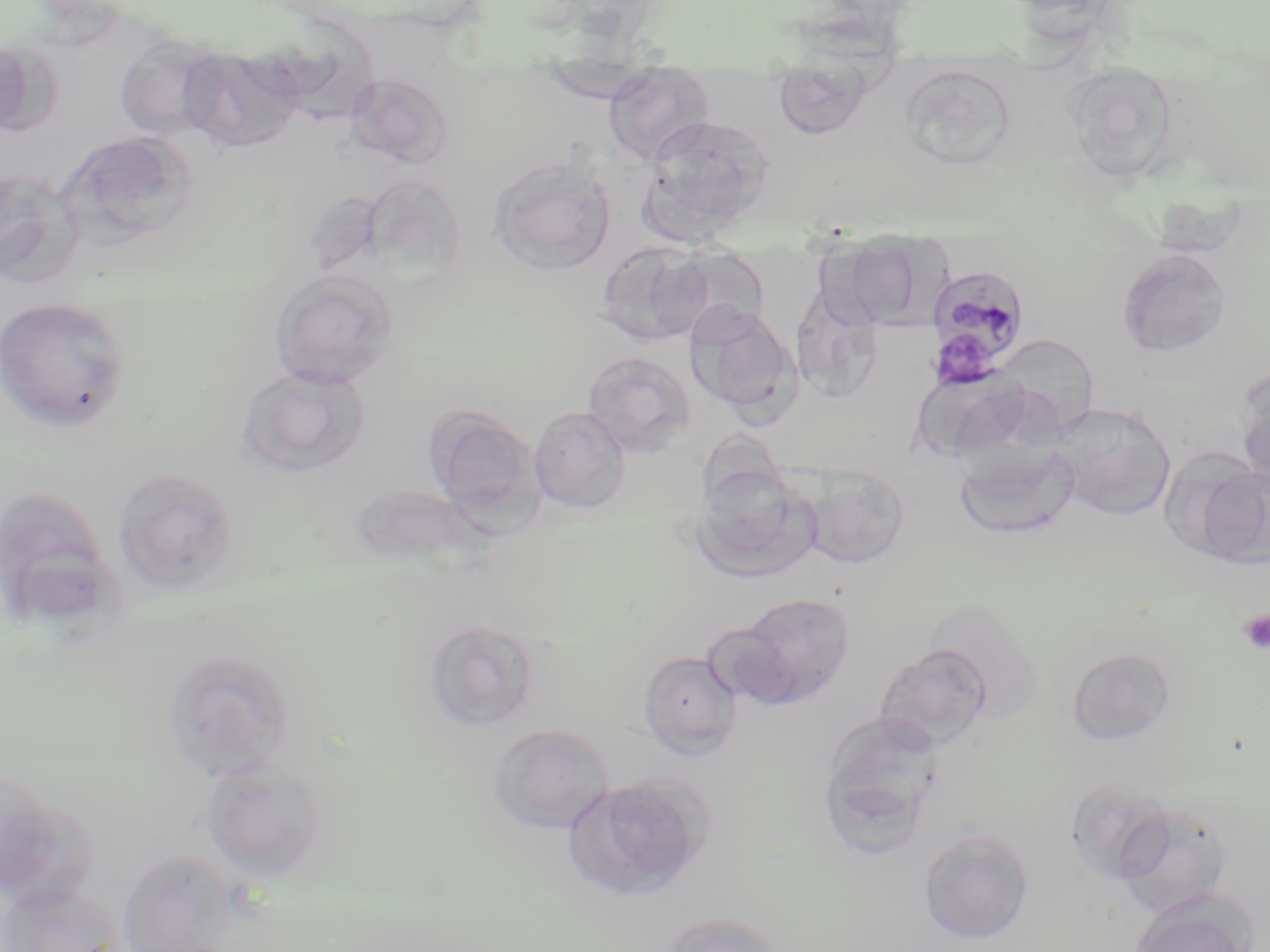

slide-level diagnosis = Plasmodium malariae
field of view = one of a larger specimen
preparation = thin blood film
uninfected red blood cell locations = approximate bounding boxes as [x1, y1, x2, y2] in pixels: [115, 33, 228, 141], [0, 39, 41, 137], [179, 45, 305, 153], [536, 64, 663, 102], [603, 66, 716, 165], [902, 66, 1014, 167], [1059, 67, 1182, 182], [772, 70, 877, 140], [343, 72, 453, 169], [641, 113, 774, 235], [61, 132, 198, 250], [488, 157, 616, 275], [0, 166, 85, 290], [361, 174, 468, 281], [827, 233, 937, 328], [595, 240, 715, 347], [590, 242, 703, 459], [1117, 247, 1233, 360], [269, 270, 399, 389], [790, 286, 885, 404], [0, 297, 130, 432], [686, 305, 802, 419], [1001, 339, 1099, 447], [583, 351, 696, 458], [237, 363, 372, 480], [1235, 366, 1270, 488], [921, 372, 1031, 471], [1053, 402, 1177, 521], [424, 405, 544, 530], [529, 406, 631, 515], [954, 441, 1080, 541], [1178, 455, 1270, 572], [800, 465, 911, 569], [112, 466, 240, 597], [689, 470, 821, 586], [346, 483, 487, 571], [0, 484, 120, 634], [736, 592, 857, 705], [921, 598, 1045, 723], [421, 618, 543, 733], [874, 644, 992, 753], [1066, 646, 1176, 746], [161, 649, 296, 781], [637, 649, 742, 759], [816, 713, 945, 859], [488, 724, 614, 834], [201, 758, 327, 883], [563, 773, 714, 904], [1064, 778, 1178, 885], [0, 786, 97, 910], [1113, 800, 1233, 917], [917, 828, 1036, 944], [117, 849, 240, 952], [0, 884, 124, 952], [1128, 891, 1258, 952], [658, 913, 790, 952]
image size = 1270×952 pixels
magnification = 1000x
Plasmodium malariae-infected red blood cell locations = approximate bounding boxes as [x1, y1, x2, y2] in pixels: [926, 263, 1030, 379]
stain = May-Grünwald-Giemsa
modality = light microscopy
platelet locations = approximate bounding boxes as [x1, y1, x2, y2] in pixels: [941, 336, 999, 388], [1238, 610, 1270, 654]